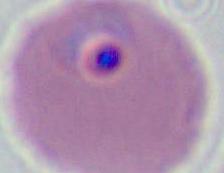

modality = photomicrograph
magnification = 400x or 1000x
identification = Plasmodium